Name the parasite shown.
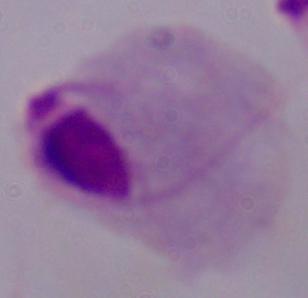
This is a trichomonad.

Photomicrograph. Captured at 1000x magnification.